Outline Plasmodium ovale parasites and classify them by life-cycle stage.
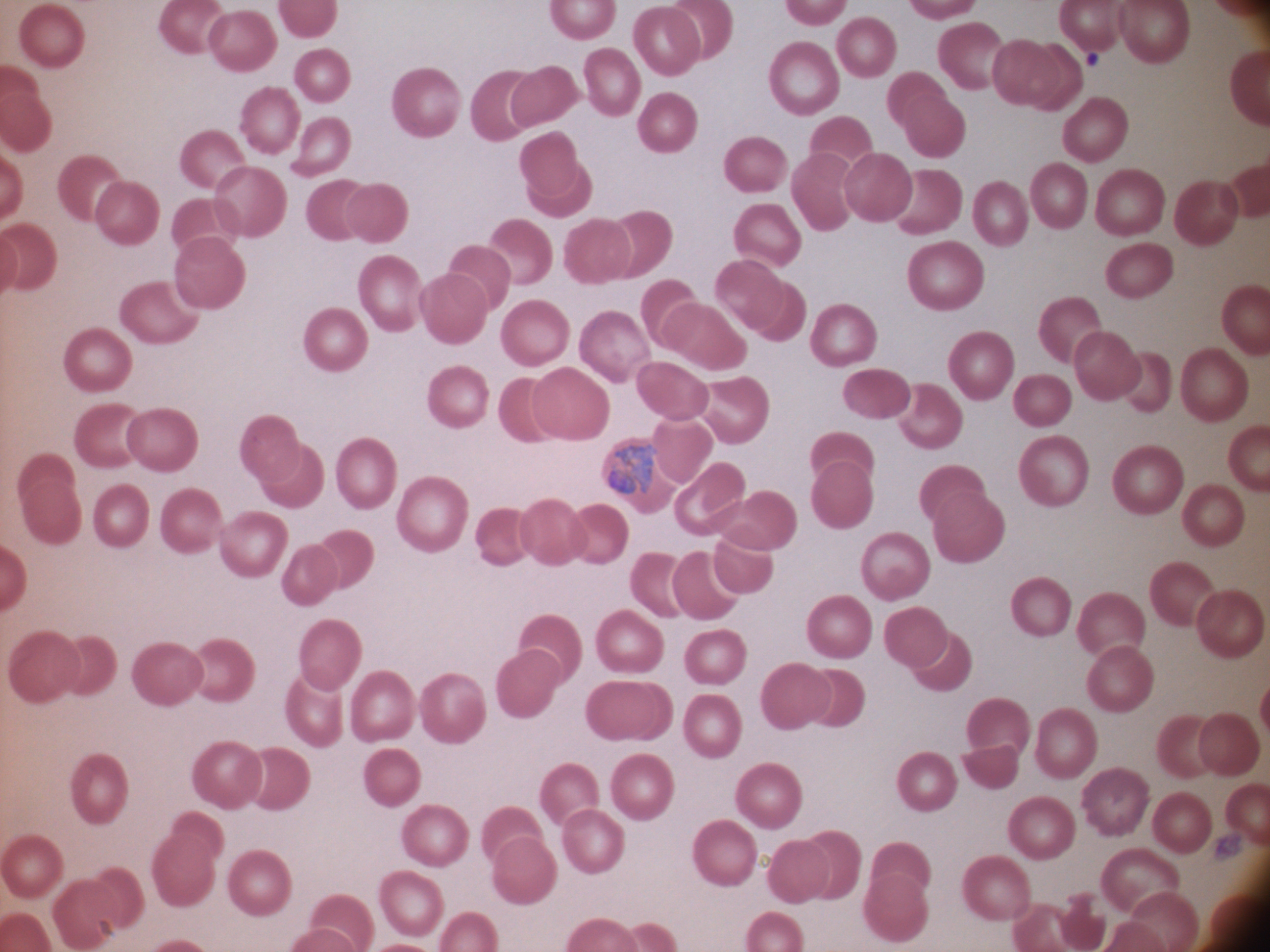
Approximate bounding boxes as [x1, y1, x2, y2] in pixels, from the source annotation, which is not necessarily exhaustive.
Trophozoites: [607, 445, 658, 495].

Giemsa stain. Thin blood film. Leica DM2000 optical microscope with a built-in camera. One field from this slide. Species: Plasmodium ovale. Image is 1270×952 pixels. Captured at 100x magnification.